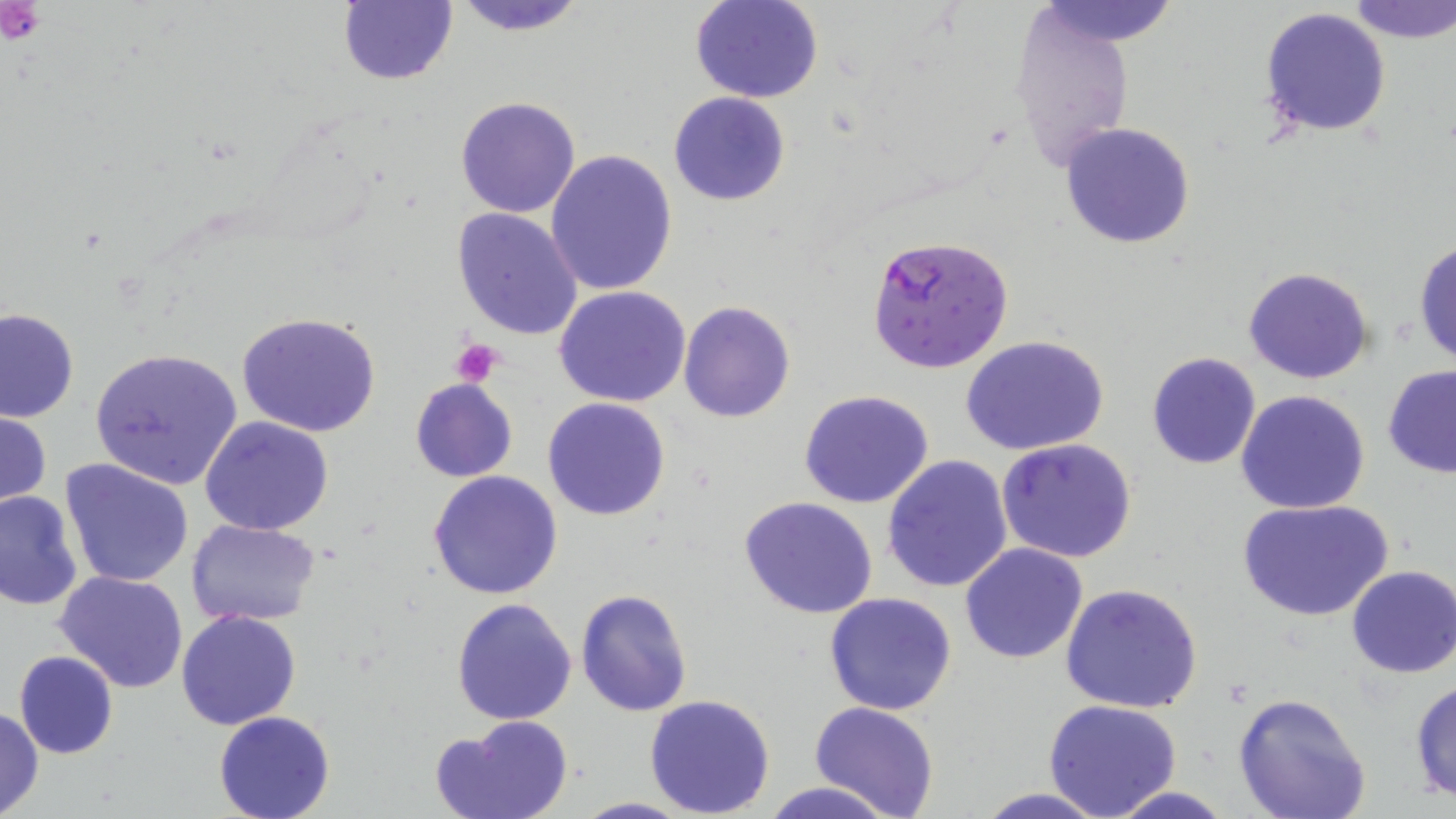

slide-level diagnosis = Plasmodium falciparum
uninfected red blood cell locations = approximate bounding boxes as [x1, y1, x2, y2] in pixels: [337, 0, 457, 86], [447, 0, 588, 37], [689, 0, 824, 103], [1032, 0, 1181, 46], [1349, 0, 1456, 44], [1259, 6, 1391, 137], [1009, 8, 1138, 173], [668, 92, 791, 206], [455, 96, 582, 219], [1059, 122, 1200, 250], [546, 150, 677, 295], [453, 206, 583, 341], [1414, 237, 1456, 369], [1244, 267, 1376, 385], [555, 286, 693, 407], [678, 300, 796, 423], [0, 307, 79, 423], [237, 312, 382, 437], [960, 334, 1110, 456], [89, 346, 244, 490], [1145, 352, 1262, 468], [1382, 364, 1456, 477], [410, 377, 519, 484], [1234, 389, 1372, 515], [798, 390, 936, 510], [542, 398, 671, 521], [0, 408, 52, 516], [200, 414, 334, 536], [996, 437, 1137, 563], [881, 454, 1014, 594], [61, 457, 195, 588], [427, 470, 564, 600], [0, 490, 83, 611], [737, 496, 882, 621], [1239, 496, 1395, 623], [186, 518, 322, 626], [960, 542, 1089, 664], [1345, 565, 1456, 679], [55, 569, 190, 696], [1060, 584, 1204, 715], [576, 589, 692, 718], [825, 592, 958, 715], [451, 596, 578, 724], [176, 608, 303, 730], [14, 650, 120, 760], [1409, 677, 1456, 803], [644, 693, 776, 818], [1229, 693, 1372, 819], [1043, 698, 1183, 818], [809, 701, 939, 819], [0, 706, 44, 816], [214, 711, 337, 819], [431, 713, 574, 819], [762, 782, 894, 819], [1108, 786, 1231, 819], [968, 788, 1116, 819], [570, 796, 697, 818]
field of view = single
magnification = 1000x
modality = light microscopy
preparation = thin blood film
Plasmodium falciparum-infected red blood cell locations = approximate bounding boxes as [x1, y1, x2, y2] in pixels: [865, 233, 1015, 375]
image size = 1456×819 pixels
platelet locations = approximate bounding boxes as [x1, y1, x2, y2] in pixels: [2, 0, 46, 46], [452, 339, 504, 387]
stain = May-Grünwald-Giemsa